Assess this cell for malaria.
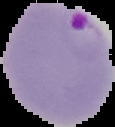

It is parasitized.

From a thin blood film. Segmented cell region on a black background. Image is 115×127 pixels.